Describe the morphology of the erythrocytes.
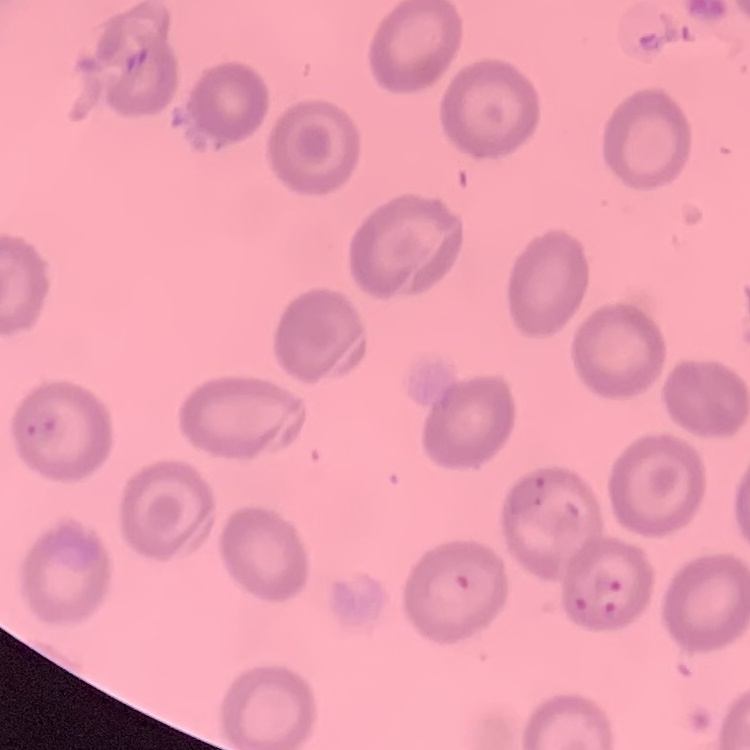
They show no rouleaux formation.

stain = Field's or Giemsa
image type = square crop of a larger photomicrograph
preparation = thin peripheral smear